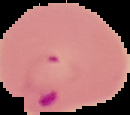
preparation = thin blood smear
image size = 130×115 pixels
result = Plasmodium parasites identified
image type = segmented cell region on a black background